Give the position of every Plasmodium parasite visible.
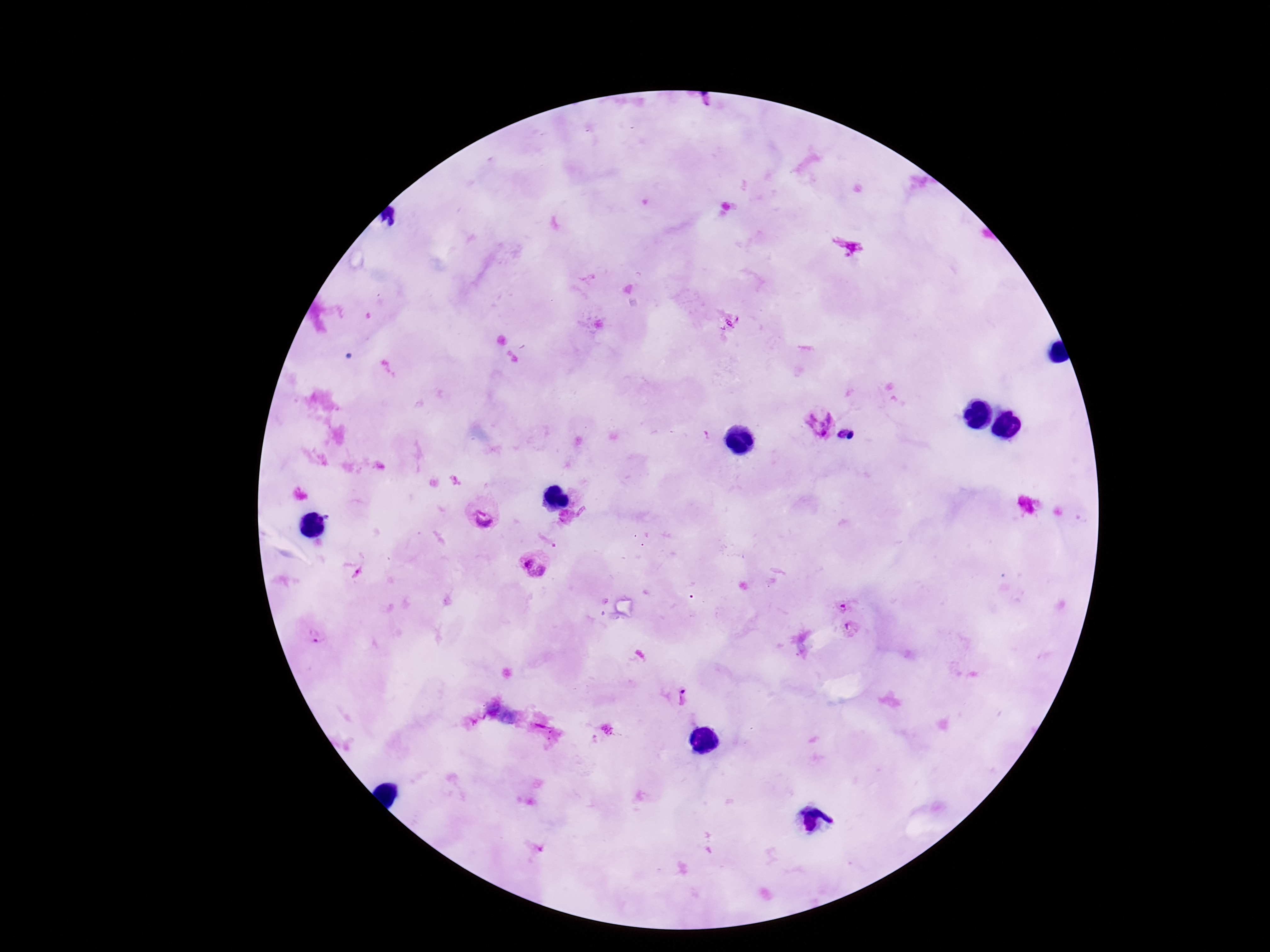

Approximate centers as {x, y} in pixels.
Plasmodium parasites: {853, 250}, {819, 422}, {844, 433}, {485, 512}, {535, 565}, {842, 601}, {853, 630}, {314, 632}, {684, 696}.

preparation = thick blood smear
patient malaria status = infected
capture = smartphone camera through the microscope eyepiece
field of view = one from this slide
image size = 1270×952 pixels
magnification = 100x
stain = Giemsa